Name the parasite shown.
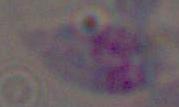

This is Toxoplasma gondii.

Captured at 1000x magnification. Photomicrograph.